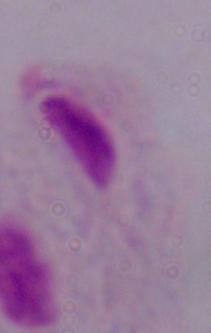
Summary:
  - Identification: trichomonad
  - Modality: photomicrograph
  - Magnification: 1000x